Name the blood parasite species.
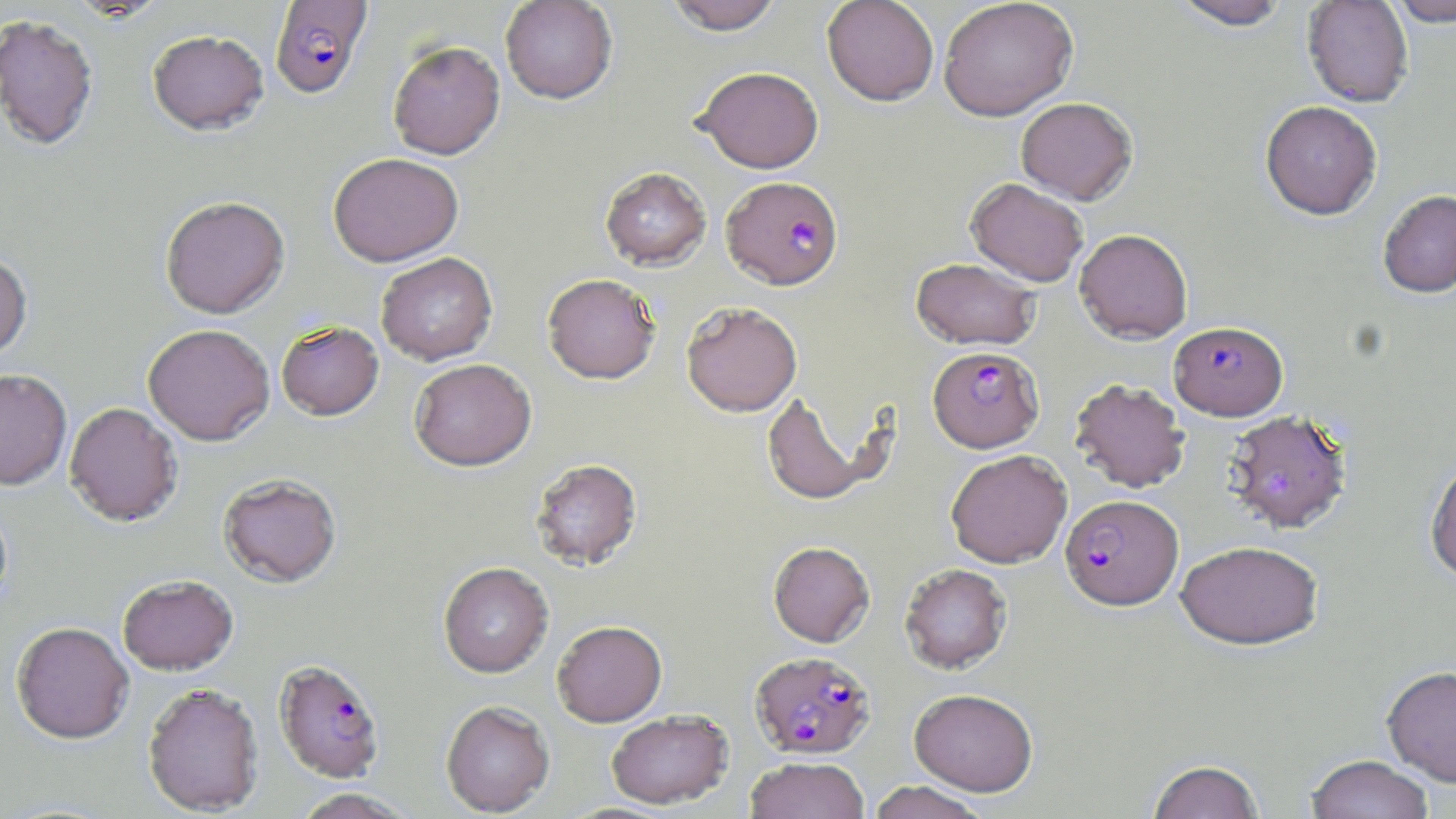
Plasmodium falciparum.

Approximate bounding boxes as (x1,y1)-(x2,y2) corner pairs in pixels. Uninfected red blood cell locations: (66,0)-(169,21), (499,0)-(618,104), (663,0)-(785,34), (822,0)-(939,105), (938,0)-(1078,121), (1169,0)-(1293,29), (1302,0)-(1414,107), (1385,0)-(1456,26), (0,14)-(99,150), (147,29)-(269,134), (387,40)-(505,159), (694,66)-(824,173), (1016,97)-(1137,204), (1260,100)-(1382,219), (328,152)-(464,266), (600,166)-(711,270), (965,177)-(1089,286), (1377,190)-(1456,297), (160,195)-(290,318), (1074,228)-(1193,343), (0,251)-(33,361), (376,252)-(497,365), (910,257)-(1040,350), (542,273)-(661,384), (681,301)-(803,416), (280,320)-(388,420), (143,323)-(275,445), (409,358)-(536,471), (0,368)-(72,489), (1069,378)-(1191,492), (762,392)-(875,506), (64,402)-(183,526), (1222,408)-(1352,534), (945,449)-(1072,568), (1424,456)-(1456,583), (530,457)-(643,570), (217,472)-(342,587), (1176,539)-(1324,650), (768,541)-(874,647), (438,562)-(554,677), (899,563)-(1012,673), (116,574)-(238,674), (552,620)-(667,726), (11,622)-(134,743), (1382,665)-(1456,787), (142,682)-(264,815), (909,687)-(1039,795), (440,700)-(555,816), (606,710)-(733,809), (1306,754)-(1434,819), (744,756)-(870,818), (1147,759)-(1264,819), (868,781)-(990,819), (290,788)-(417,818). Plasmodium falciparum-infected red blood cell locations: (270,1)-(371,98), (722,175)-(843,289), (1169,321)-(1287,420), (928,346)-(1044,452), (1060,494)-(1183,610), (750,650)-(875,759), (273,658)-(386,782). Platelet locations: (1263,468)-(1299,501). Thin blood film. One field of a larger specimen. Optical microscopy. Captured at 1000x magnification. May-Grünwald-Giemsa-stained preparation. Image is 1456×819 pixels.